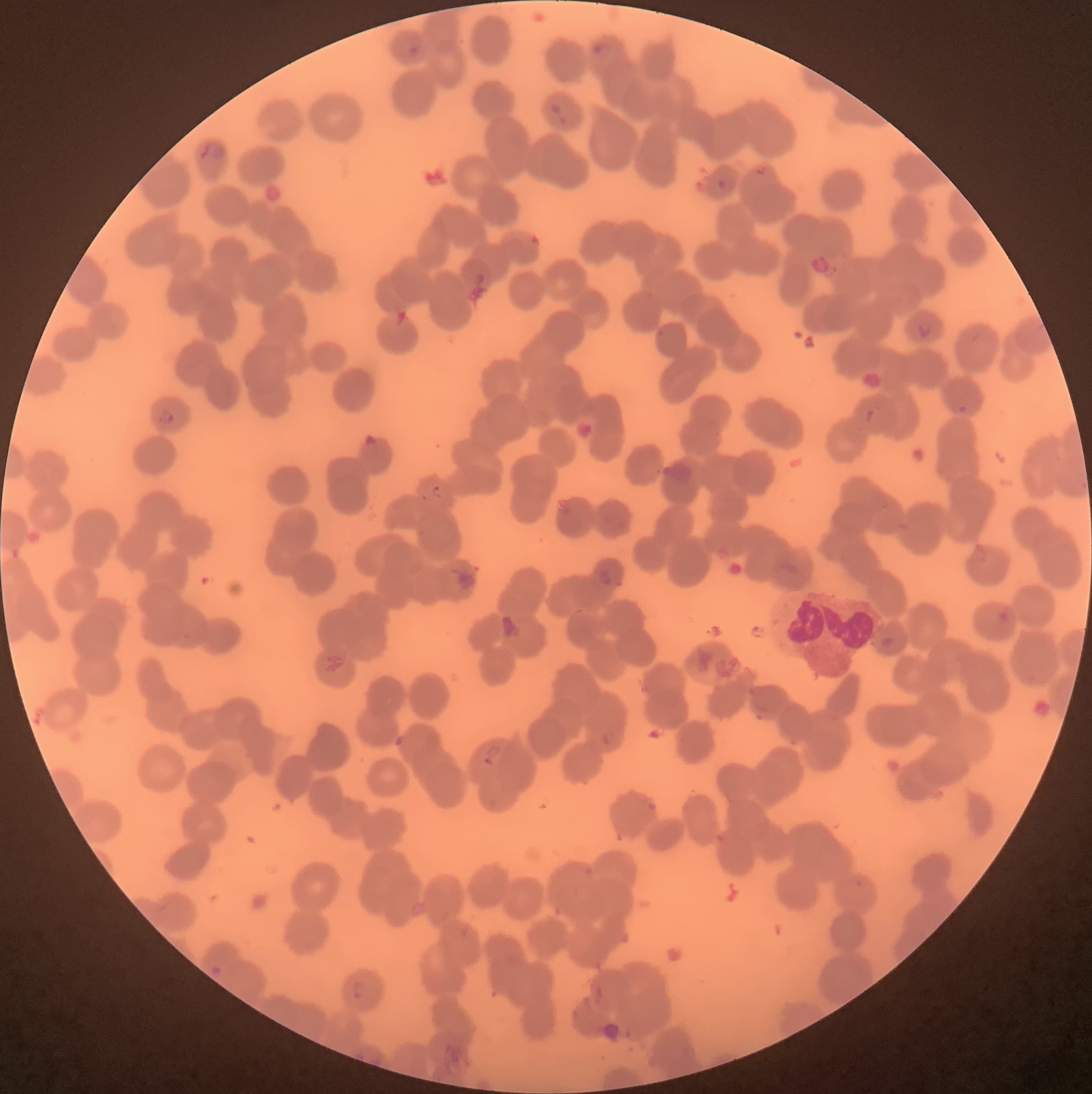
coordinate format = approximate bounding boxes as (x1,y1)-(x2,y2) corner pairs in pixels
Plasmodium parasite locations = (589,41)-(609,60), (406,44)-(422,59), (550,104)-(566,127), (198,142)-(225,161), (716,179)-(726,190), (914,322)-(934,340), (956,404)-(968,414), (865,405)-(878,420), (157,407)-(175,426), (362,434)-(380,456), (430,485)-(444,501), (597,569)-(614,586), (481,744)-(500,765), (350,978)-(367,1003)
white blood cell locations = (763,586)-(876,682)
modality = optical microscopy
preparation = thin blood film
image size = 1092×1094 pixels
red blood cell morphology = rouleaux formation